Classify this cell by malaria status.
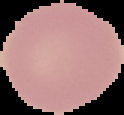

Uninfected.

preparation = thin blood film
image type = segmented cell region with the area outside set to black
image size = 124×115 pixels